Locate every blood parasite and identify its species.
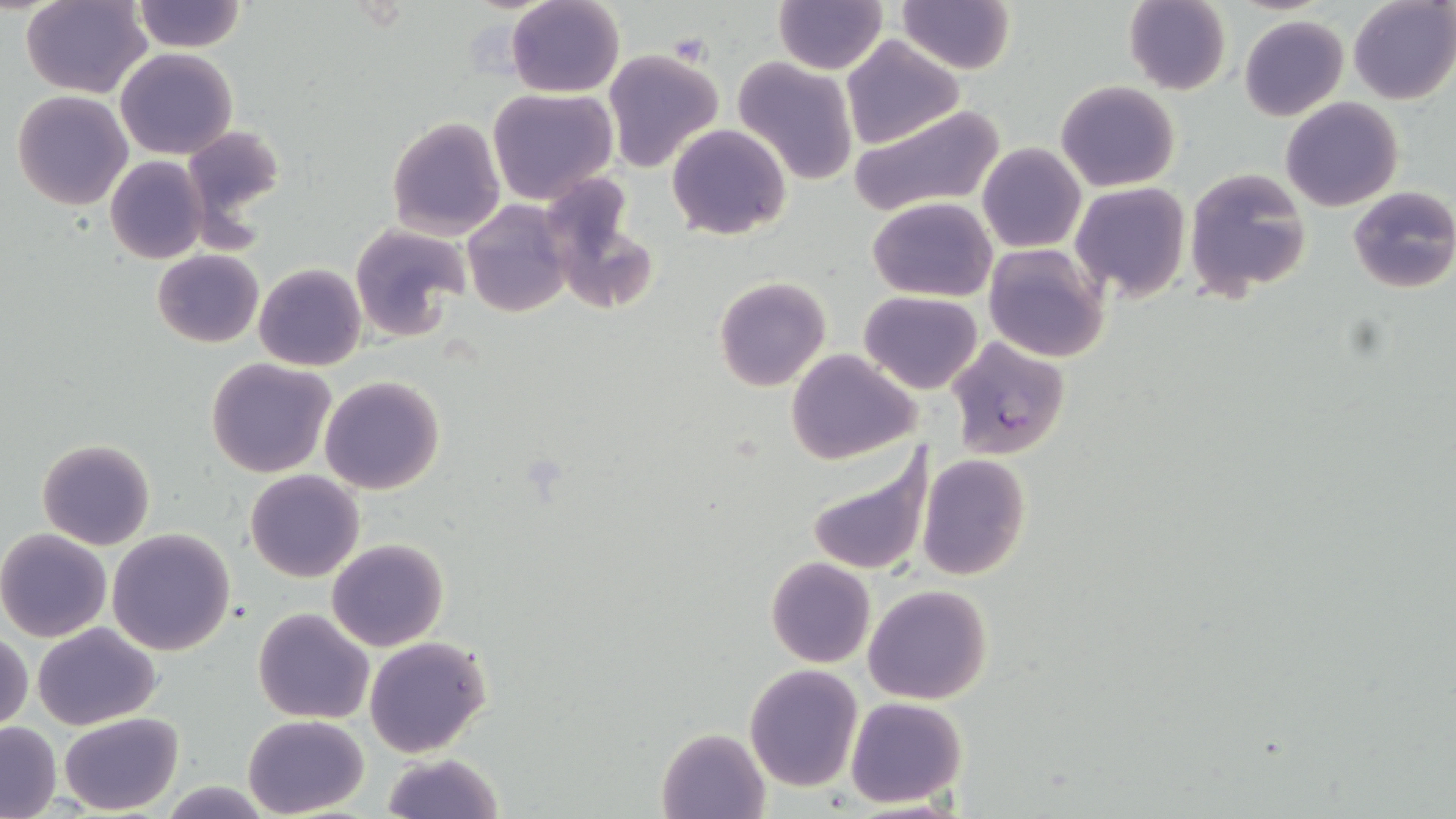
Approximate bounding boxes as (x1, y1, x2, y2) in pixels.
Plasmodium falciparum-infected red blood cells: (945, 336, 1070, 460).
No Plasmodium ovale, Plasmodium malariae, Plasmodium vivax, Babesia divergens, or Trypanosoma brucei observed.

Summary:
  - Uninfected red blood cell locations: (22, 0, 150, 98), (132, 0, 247, 53), (1124, 0, 1231, 94), (1347, 0, 1456, 104), (506, 1, 625, 96), (897, 1, 1015, 75), (774, 2, 886, 73), (1238, 14, 1350, 121), (841, 35, 963, 147), (602, 48, 724, 172), (116, 49, 238, 159), (732, 56, 860, 184), (1056, 80, 1181, 191), (487, 87, 618, 203), (11, 90, 133, 211), (1280, 97, 1403, 211), (846, 104, 1005, 222), (386, 116, 506, 238), (668, 123, 790, 240), (183, 125, 286, 225), (977, 143, 1085, 253), (105, 155, 208, 264), (1184, 168, 1311, 301), (540, 177, 657, 314), (1071, 182, 1192, 302), (1348, 185, 1456, 295), (867, 196, 997, 302), (462, 200, 572, 317), (350, 223, 472, 344), (983, 242, 1110, 362), (152, 249, 262, 348), (254, 263, 366, 371), (714, 275, 831, 392), (858, 291, 983, 394), (785, 348, 920, 464), (206, 359, 336, 477), (320, 377, 445, 495), (36, 439, 157, 550), (803, 446, 932, 579), (917, 453, 1031, 581), (245, 469, 364, 582), (106, 528, 236, 656), (0, 529, 113, 642), (327, 538, 448, 652), (765, 557, 876, 668), (863, 584, 992, 705), (253, 607, 374, 724), (32, 622, 160, 730), (1, 631, 32, 734), (364, 634, 491, 757), (744, 663, 864, 791), (845, 696, 967, 808), (58, 712, 182, 815), (243, 714, 368, 817), (0, 721, 61, 818), (657, 728, 769, 818), (380, 752, 504, 819)
  - Slide-level diagnosis: Plasmodium falciparum
  - Stain: May-Grünwald-Giemsa
  - Preparation: thin blood film
  - Magnification: 1000x
  - Image size: 1456×819 pixels
  - Modality: light microscopy
  - Field of view: single